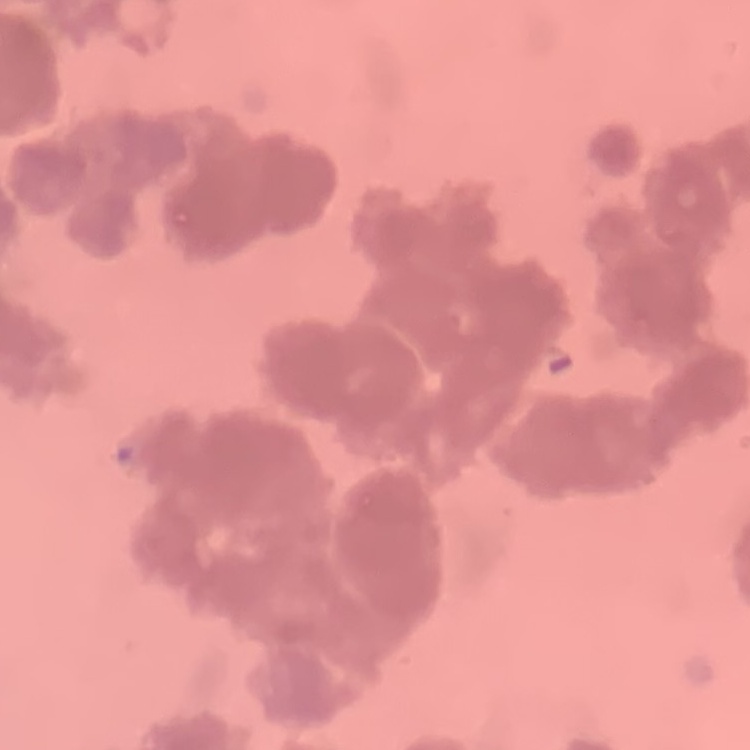

erythrocyte morphology = rouleaux formation
image type = one tile cut from a larger photomicrograph
stain = Field's or Giemsa
preparation = thin blood film